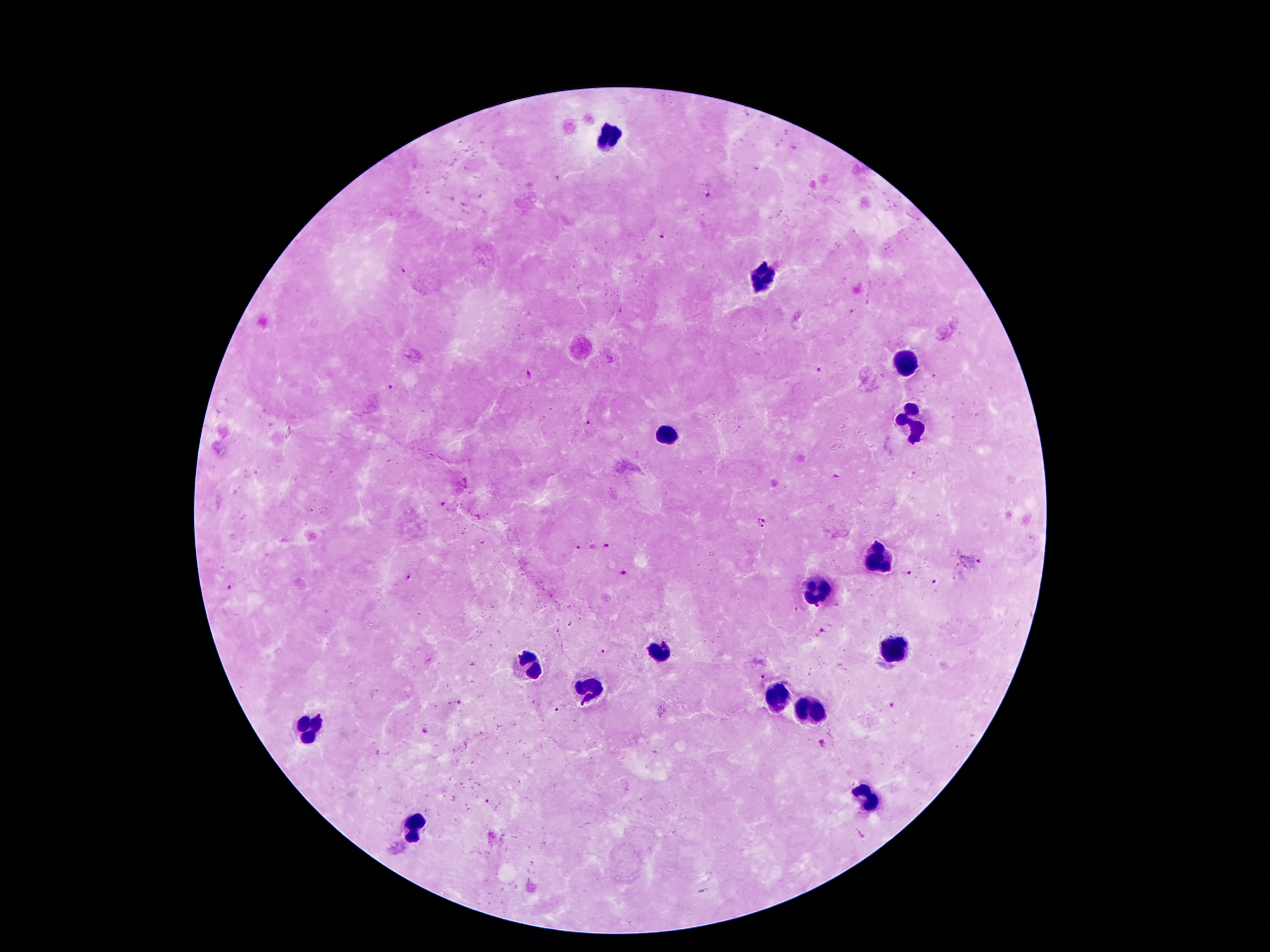
Approximate centers as [x, y] in pixels.
Summary:
  - Malaria parasite locations: [708, 196], [661, 235], [403, 270], [609, 359], [816, 370], [528, 375], [933, 376], [392, 387], [587, 423], [835, 475], [442, 504], [763, 523], [607, 546], [577, 548], [982, 562], [624, 572], [906, 573], [408, 579], [934, 583], [228, 589], [822, 630], [602, 651], [763, 676], [891, 704], [556, 709], [424, 730], [822, 742], [488, 801], [860, 834]
  - Leukocyte locations: [608, 139], [757, 281], [902, 359], [908, 418], [667, 433], [873, 561], [816, 590], [894, 649], [661, 651], [526, 668], [583, 691], [778, 697], [810, 714], [310, 731], [864, 800], [413, 827]
  - Capture: smartphone through the microscope eyepiece
  - Field of view: one from this slide
  - Magnification: 100x
  - Image size: 1270×952 pixels
  - Preparation: thick blood film
  - Stain: Giemsa
  - Patient malaria status: positive for Plasmodium falciparum